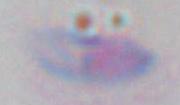

Summary:
  - Magnification: 1000x
  - Modality: micrograph
  - Identification: Toxoplasma gondii